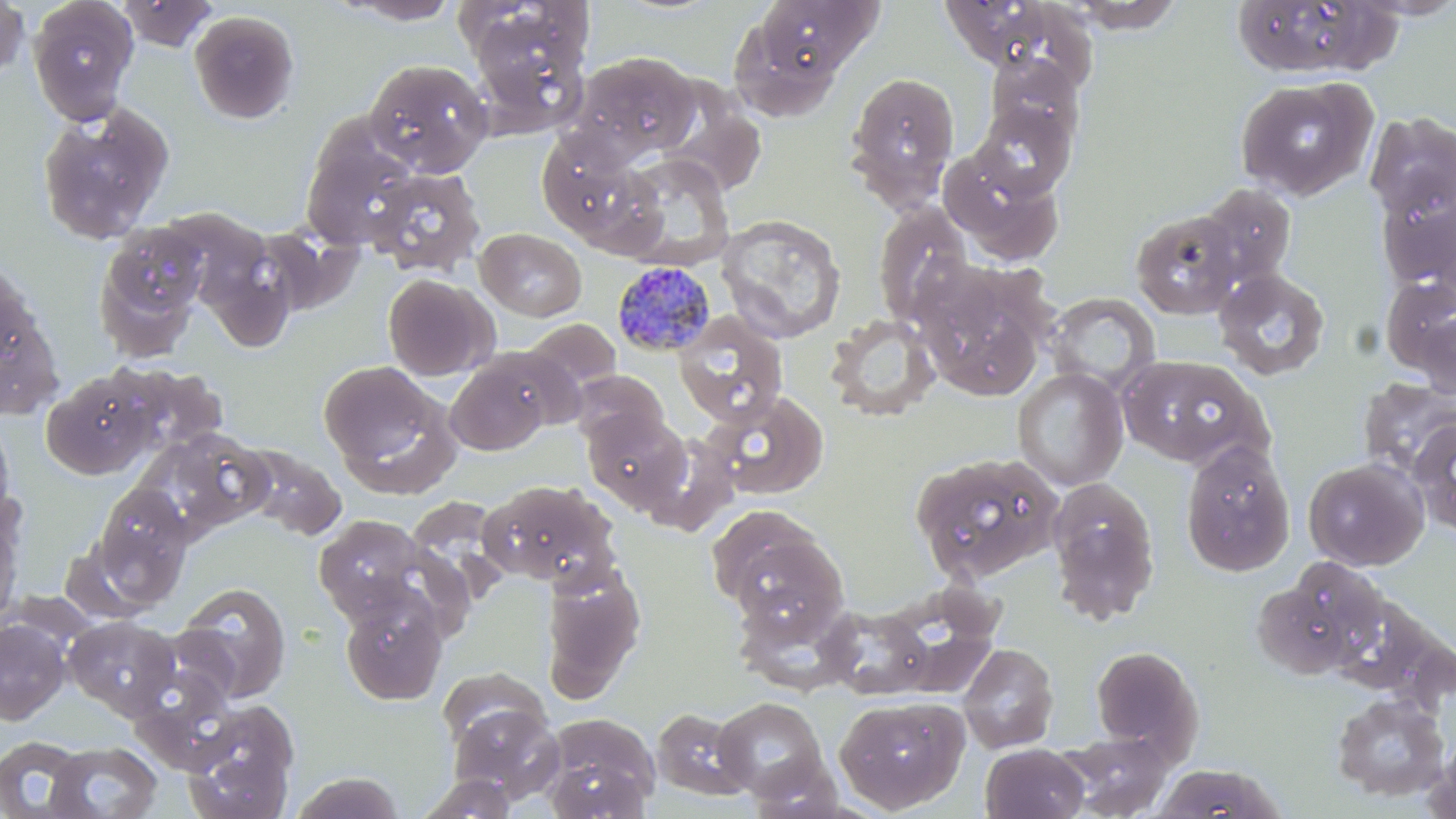
Summary:
  - Coordinate format: approximate bounding boxes as (x1, y1, x2, y2) in pixels
  - Uninfected red blood cell locations: (0, 0, 29, 84), (27, 0, 139, 125), (116, 0, 221, 52), (331, 0, 466, 26), (1229, 0, 1397, 80), (746, 1, 884, 83), (936, 1, 1074, 74), (1061, 1, 1186, 33), (465, 4, 595, 137), (727, 8, 850, 121), (188, 9, 301, 124), (570, 51, 701, 162), (985, 55, 1086, 150), (364, 58, 493, 177), (845, 70, 960, 206), (1235, 77, 1377, 201), (973, 101, 1076, 198), (36, 102, 175, 245), (1365, 111, 1456, 226), (301, 121, 422, 251), (536, 133, 655, 244), (939, 148, 1064, 266), (617, 153, 734, 269), (366, 167, 485, 278), (1378, 178, 1456, 298), (1194, 181, 1297, 292), (872, 201, 974, 325), (276, 203, 378, 313), (192, 206, 298, 356), (1131, 209, 1242, 320), (715, 214, 847, 344), (95, 219, 209, 349), (474, 227, 587, 321), (1213, 268, 1331, 381), (918, 273, 1053, 399), (382, 274, 497, 381), (0, 281, 62, 419), (1045, 292, 1161, 394), (1409, 303, 1456, 401), (672, 311, 788, 429), (824, 313, 942, 422), (523, 319, 622, 398), (444, 352, 560, 456), (1117, 354, 1267, 470), (318, 360, 453, 489), (118, 364, 229, 458), (1011, 368, 1129, 490), (570, 370, 670, 451), (41, 372, 159, 479), (1357, 377, 1456, 481), (706, 391, 828, 499), (583, 409, 691, 514), (0, 415, 16, 526), (1411, 419, 1456, 537), (133, 428, 269, 541), (637, 434, 738, 534), (1180, 440, 1295, 577), (236, 444, 347, 541), (908, 450, 1064, 585), (1303, 457, 1428, 571), (1046, 479, 1160, 625), (477, 480, 618, 588), (91, 482, 193, 600), (0, 500, 24, 629), (706, 505, 846, 629), (313, 514, 431, 623), (1252, 559, 1386, 681), (539, 562, 646, 703), (174, 581, 293, 703), (338, 588, 448, 706), (733, 596, 870, 691), (820, 605, 933, 700), (62, 615, 180, 719), (0, 618, 71, 725), (958, 642, 1059, 754), (1090, 645, 1203, 759), (1330, 693, 1450, 802), (834, 695, 970, 814), (712, 697, 829, 801), (448, 698, 565, 801), (182, 699, 301, 818), (651, 706, 756, 802), (540, 717, 661, 818), (1057, 732, 1173, 817), (0, 735, 91, 819), (1426, 735, 1456, 819), (44, 741, 163, 818), (981, 743, 1089, 819), (745, 754, 848, 818), (1149, 763, 1286, 819), (290, 771, 405, 818), (416, 773, 518, 818)
  - Plasmodium malariae-infected red blood cell locations: (612, 260, 717, 358)
  - Slide-level diagnosis: Plasmodium malariae
  - Image size: 1456×819 pixels
  - Magnification: 1000x
  - Stain: May-Grünwald-Giemsa
  - Modality: optical microscopy
  - Preparation: thin blood film
  - Field of view: single